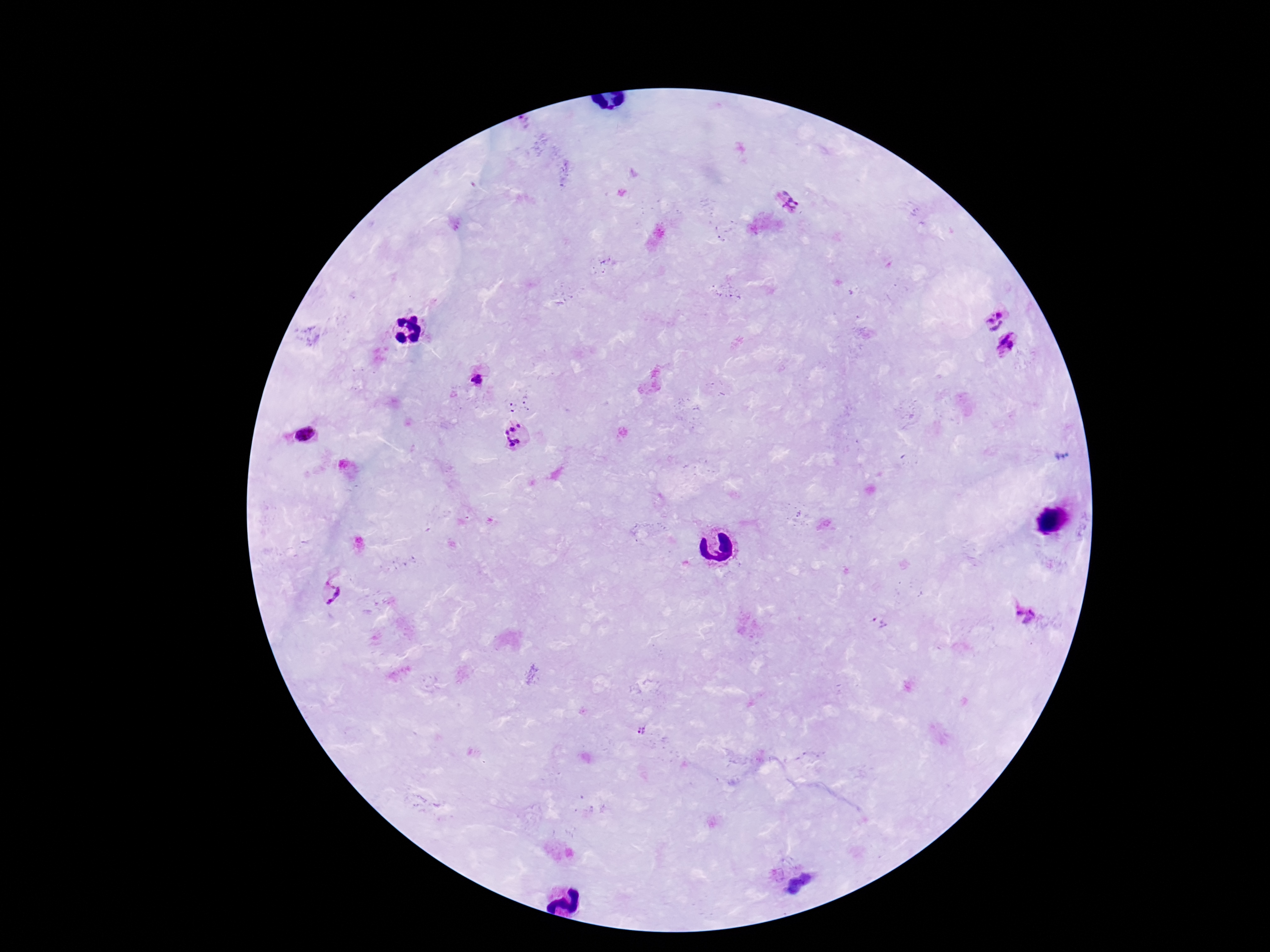

Approximate centers as [x, y] in pixels.
Summary:
  - Plasmodium parasite locations: [788, 201], [993, 317], [1008, 344], [479, 381], [514, 432], [304, 434], [331, 591], [1025, 614], [878, 623], [641, 732]
  - Magnification: 100x
  - Capture: smartphone camera through the microscope eyepiece
  - Field of view: single
  - Stain: Giemsa
  - Patient malaria status: infected
  - Image size: 1270×952 pixels
  - Preparation: thick peripheral-blood smear